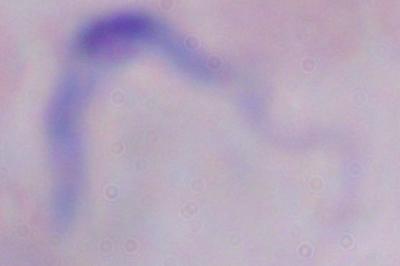
modality = micrograph
identification = trypanosome
magnification = 1000x